Classify this cell by malaria status.
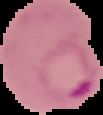

It is parasitized.

Summary:
  - Preparation: thin blood smear
  - Image size: 103×115 pixels
  - Image type: segmented cell region on a black background